Assess this cell for malaria.
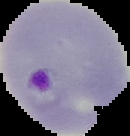

It is parasitized.

From a thin blood smear. Image is 130×136 pixels. Cell region segmented out of the field of view; the surrounding area is masked to black.